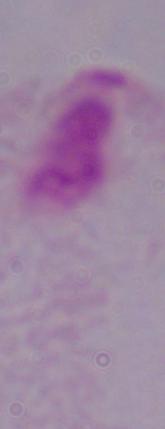

Summary:
  - Identification: trichomonad
  - Modality: micrograph
  - Magnification: 1000x